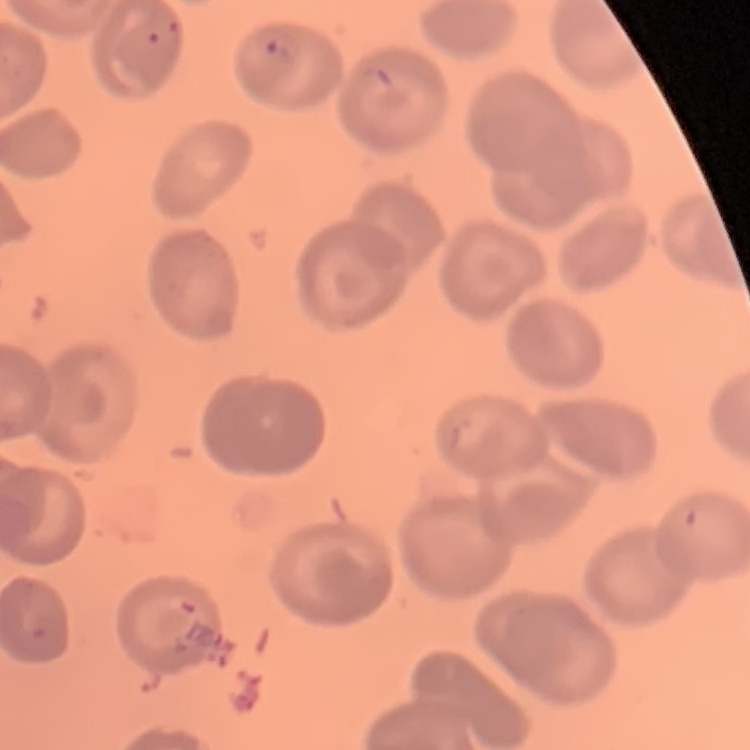

red blood cell morphology = no rouleaux formation
stain = Field's or Giemsa
preparation = thin peripheral smear
image type = square crop of a larger photomicrograph